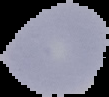
image_type: segmented cell region with the area outside set to black
malaria_status: uninfected
preparation: thin blood smear
image_size: 109×97 pixels